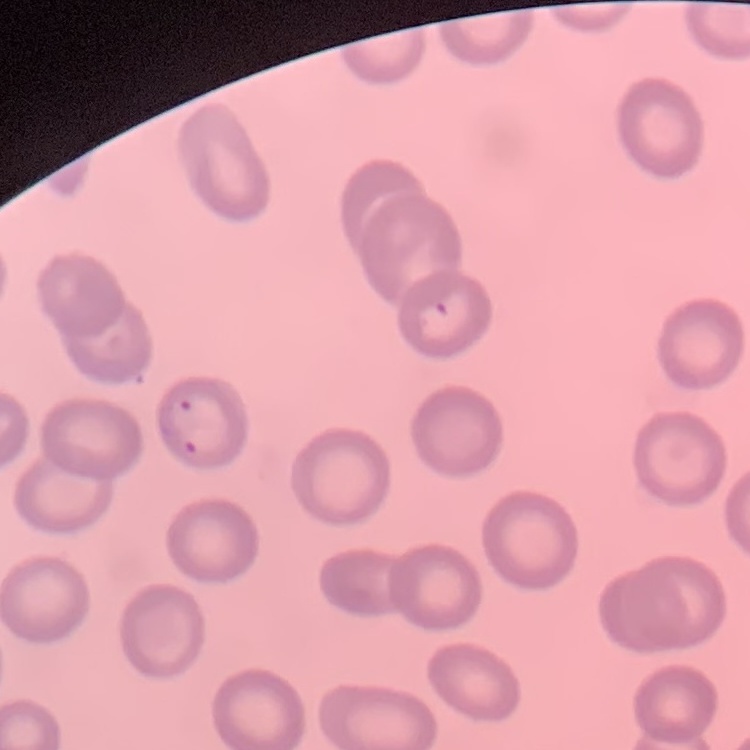
Summary:
  - Red blood cell morphology: no rouleaux formation
  - Image type: one tile cut from a larger photomicrograph
  - Preparation: thin blood smear
  - Stain: Field's or Giemsa